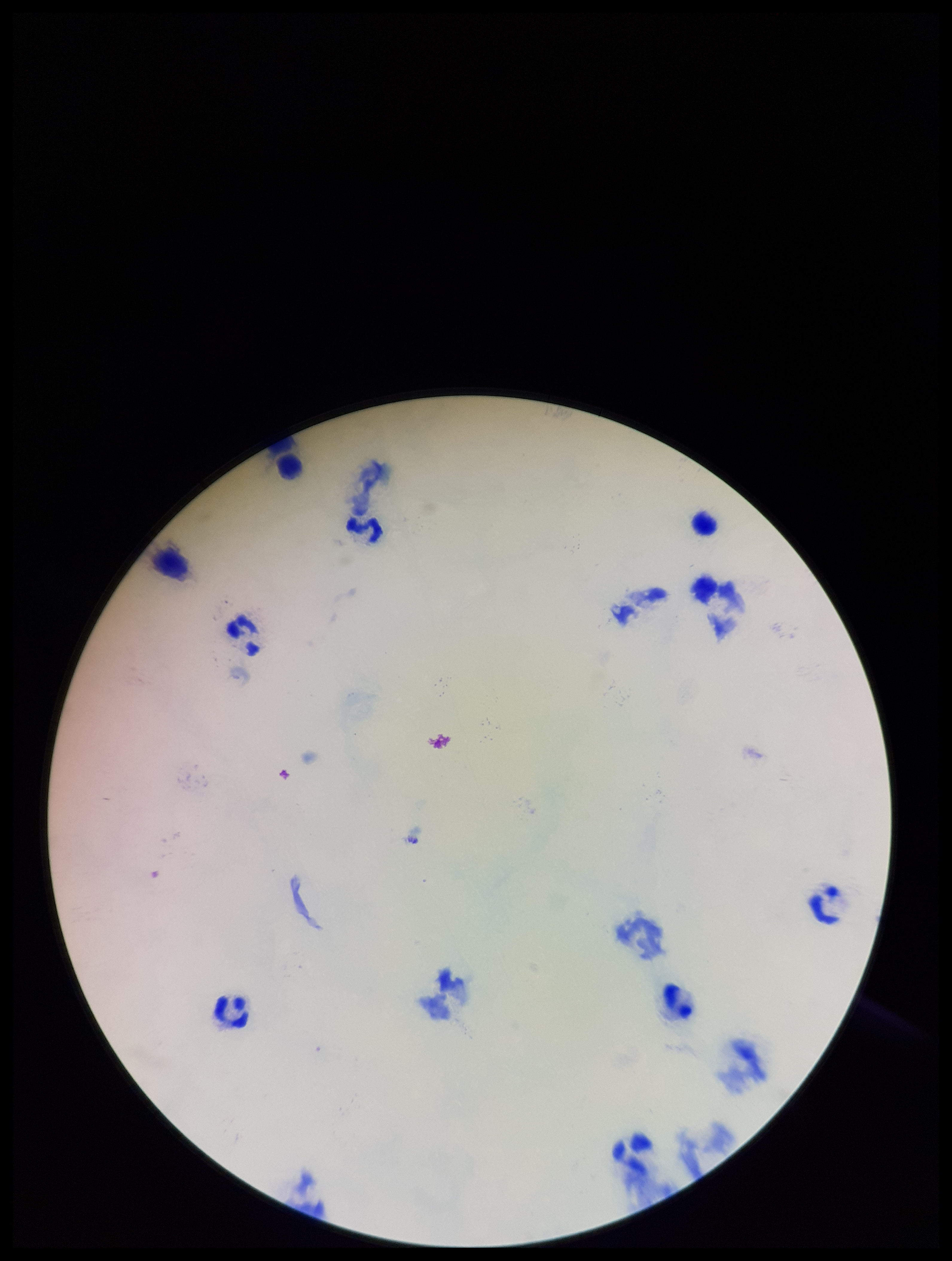 Stained with Giemsa. Patient malaria status: negative. Preparation: thick. Image is 952×1261 pixels. Parasite count: 0. Plasmodium parasites: none seen. Leukocyte count: 9. One field from this slide. Smartphone photograph taken through the eyepiece of a microscope.